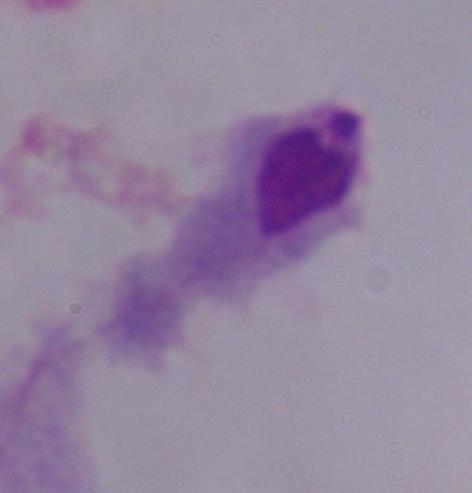 A trichomonad is shown. Photomicrograph. 1000x magnification.